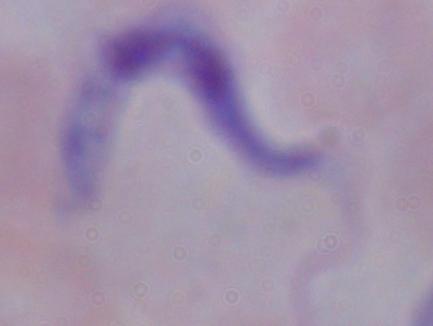
modality = micrograph
identification = trypanosome
magnification = 1000x